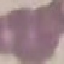
Summary:
  - Result: no malaria parasites seen
  - Preparation: thin blood smear
  - Stain: Giemsa
  - Capture: smartphone through the microscope eyepiece
  - Image type: cell patch, automatically extracted from a larger field of view and resized to 64 × 64 pixels